Name the parasite shown.
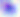
This is Toxoplasma gondii.

modality = photomicrograph
magnification = 400x